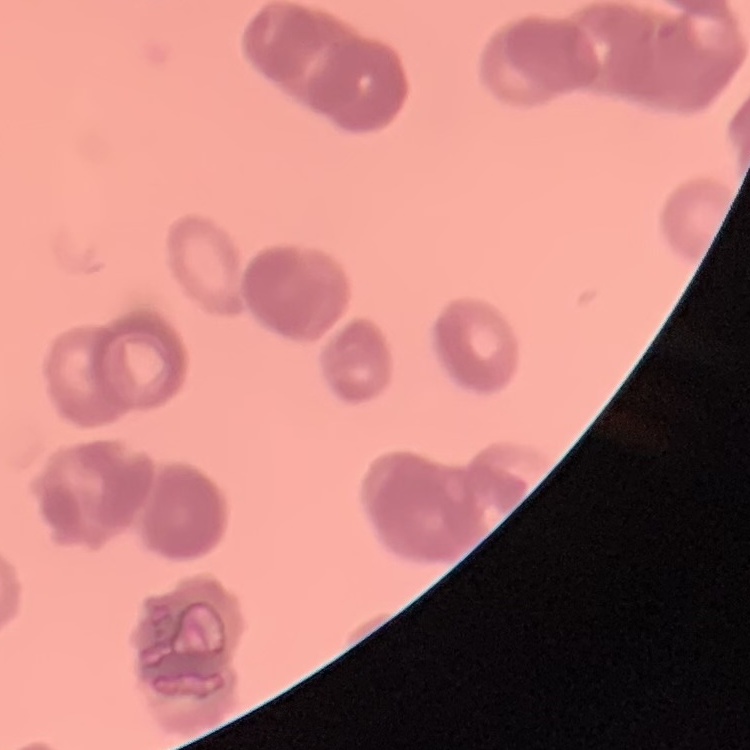

Summary:
  - Erythrocyte morphology: rouleaux formation
  - Preparation: thin blood smear
  - Stain: Field's or Giemsa
  - Image type: square crop of a larger photomicrograph